Assess this cell for malaria.
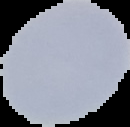

It is uninfected.

Summary:
  - Image type: segmented cell region with the area outside set to black
  - Image size: 130×127 pixels
  - Preparation: thin blood film